Report the malaria status of this cell.
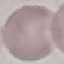
It is uninfected.

Thin blood film. Giemsa stain. Automatically extracted cell patch, resized to 64 × 64 pixels. Acquired by smartphone through the microscope eyepiece.